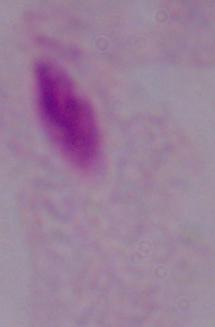

identification = trichomonad
magnification = 1000x
modality = photomicrograph